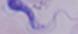 A trypanosome is seen. Captured at 1000x magnification. Micrograph.